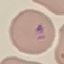
result = malaria parasites detected
capture = smartphone camera at the microscope eyepiece
image type = automatically extracted cell patch, resized to 64 × 64 pixels
stain = Giemsa
preparation = thin blood film